Outline each blood parasite and name the species.
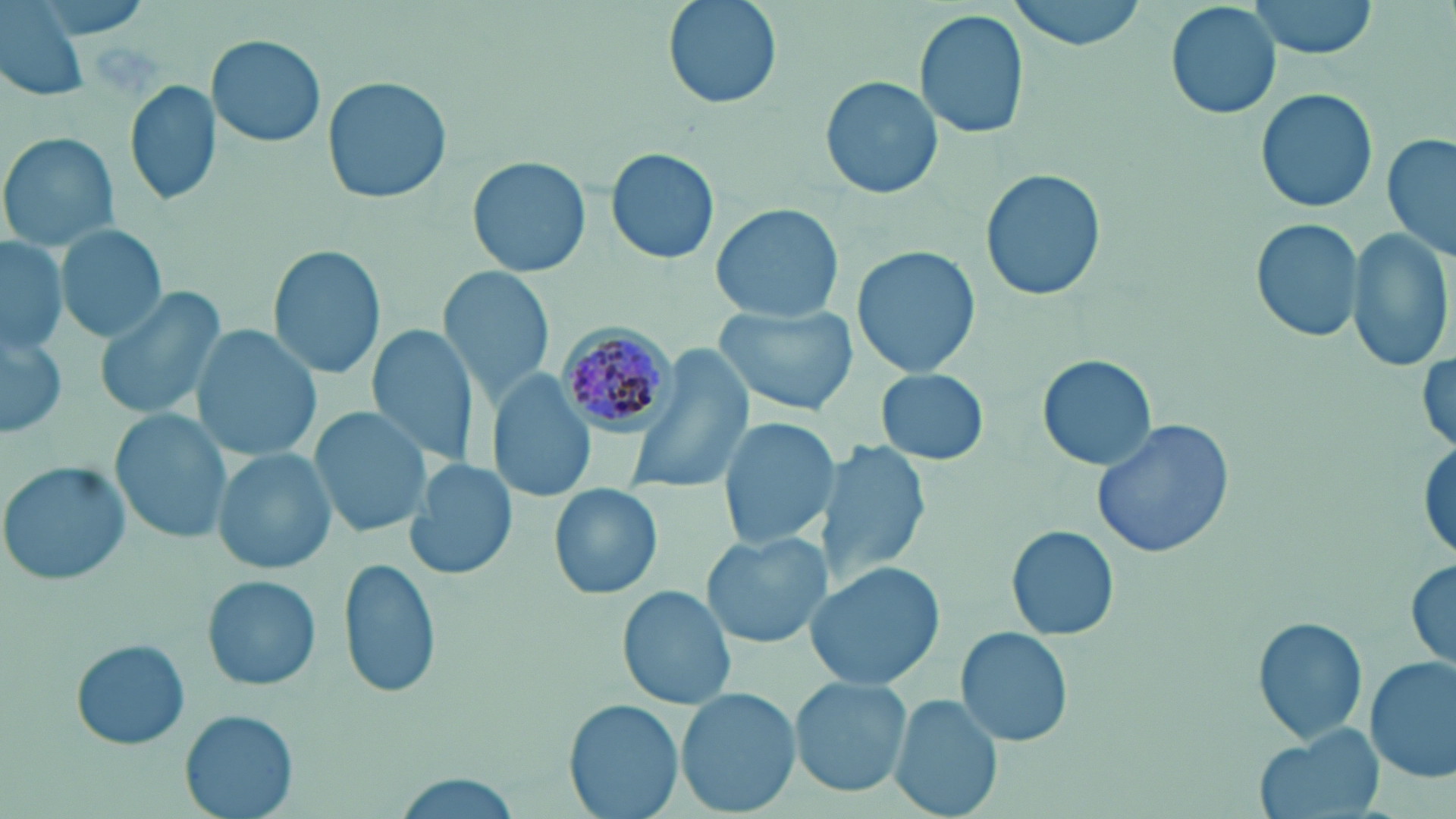

Approximate bounding boxes as named x1/y1/x2/y2 corners in pixels.
Plasmodium malariae-infected red blood cells: (x1=555, y1=325, x2=676, y2=435).
No Plasmodium falciparum, Plasmodium ovale, Plasmodium vivax, Babesia divergens, or Trypanosoma brucei observed.

slide-level diagnosis = Plasmodium malariae
modality = light microscopy
stain = May-Grünwald-Giemsa
magnification = 1000x
field of view = one of a larger specimen
uninfected red blood cell locations = approximate bounding boxes as named x1/y1/x2/y2 corners in pixels: (x1=663, y1=0, x2=782, y2=110), (x1=1007, y1=0, x2=1148, y2=50), (x1=1166, y1=0, x2=1281, y2=119), (x1=1248, y1=0, x2=1382, y2=59), (x1=1, y1=3, x2=92, y2=102), (x1=916, y1=8, x2=1030, y2=140), (x1=206, y1=34, x2=328, y2=147), (x1=321, y1=75, x2=452, y2=207), (x1=821, y1=75, x2=943, y2=201), (x1=125, y1=79, x2=222, y2=208), (x1=1254, y1=88, x2=1379, y2=213), (x1=2, y1=132, x2=117, y2=252), (x1=1382, y1=134, x2=1455, y2=264), (x1=607, y1=147, x2=720, y2=265), (x1=466, y1=156, x2=593, y2=279), (x1=981, y1=170, x2=1106, y2=302), (x1=709, y1=203, x2=843, y2=321), (x1=1248, y1=215, x2=1363, y2=344), (x1=55, y1=223, x2=168, y2=342), (x1=1350, y1=227, x2=1453, y2=372), (x1=1, y1=236, x2=67, y2=352), (x1=267, y1=242, x2=386, y2=380), (x1=852, y1=247, x2=980, y2=376), (x1=442, y1=268, x2=554, y2=399), (x1=94, y1=283, x2=225, y2=423), (x1=719, y1=302, x2=862, y2=415), (x1=366, y1=323, x2=482, y2=470), (x1=191, y1=325, x2=323, y2=463), (x1=0, y1=333, x2=68, y2=439), (x1=626, y1=350, x2=753, y2=496), (x1=1038, y1=354, x2=1158, y2=472), (x1=876, y1=368, x2=989, y2=465), (x1=487, y1=374, x2=596, y2=502), (x1=310, y1=406, x2=432, y2=540), (x1=111, y1=408, x2=232, y2=544), (x1=719, y1=417, x2=837, y2=550), (x1=1089, y1=417, x2=1237, y2=561), (x1=1412, y1=431, x2=1456, y2=567), (x1=819, y1=439, x2=931, y2=588), (x1=213, y1=449, x2=336, y2=575), (x1=406, y1=458, x2=515, y2=581), (x1=1, y1=460, x2=131, y2=587), (x1=550, y1=482, x2=659, y2=601), (x1=1006, y1=524, x2=1120, y2=642), (x1=700, y1=531, x2=827, y2=650), (x1=1404, y1=554, x2=1456, y2=673), (x1=337, y1=557, x2=442, y2=699), (x1=808, y1=561, x2=946, y2=690), (x1=202, y1=573, x2=322, y2=691), (x1=620, y1=581, x2=736, y2=709), (x1=1250, y1=614, x2=1370, y2=747), (x1=956, y1=626, x2=1073, y2=748), (x1=71, y1=640, x2=190, y2=750), (x1=1366, y1=655, x2=1454, y2=783), (x1=790, y1=676, x2=911, y2=797), (x1=676, y1=687, x2=801, y2=818), (x1=889, y1=692, x2=1004, y2=819), (x1=565, y1=699, x2=684, y2=819), (x1=180, y1=710, x2=299, y2=819), (x1=1252, y1=724, x2=1385, y2=819), (x1=391, y1=776, x2=522, y2=817)
preparation = thin blood film
image size = 1456×819 pixels